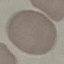

Result: negative for malaria parasites. Thin blood film. Giemsa-stained preparation. Acquired by smartphone through the microscope eyepiece. Automatically extracted cell patch, resized to 64 × 64 pixels.